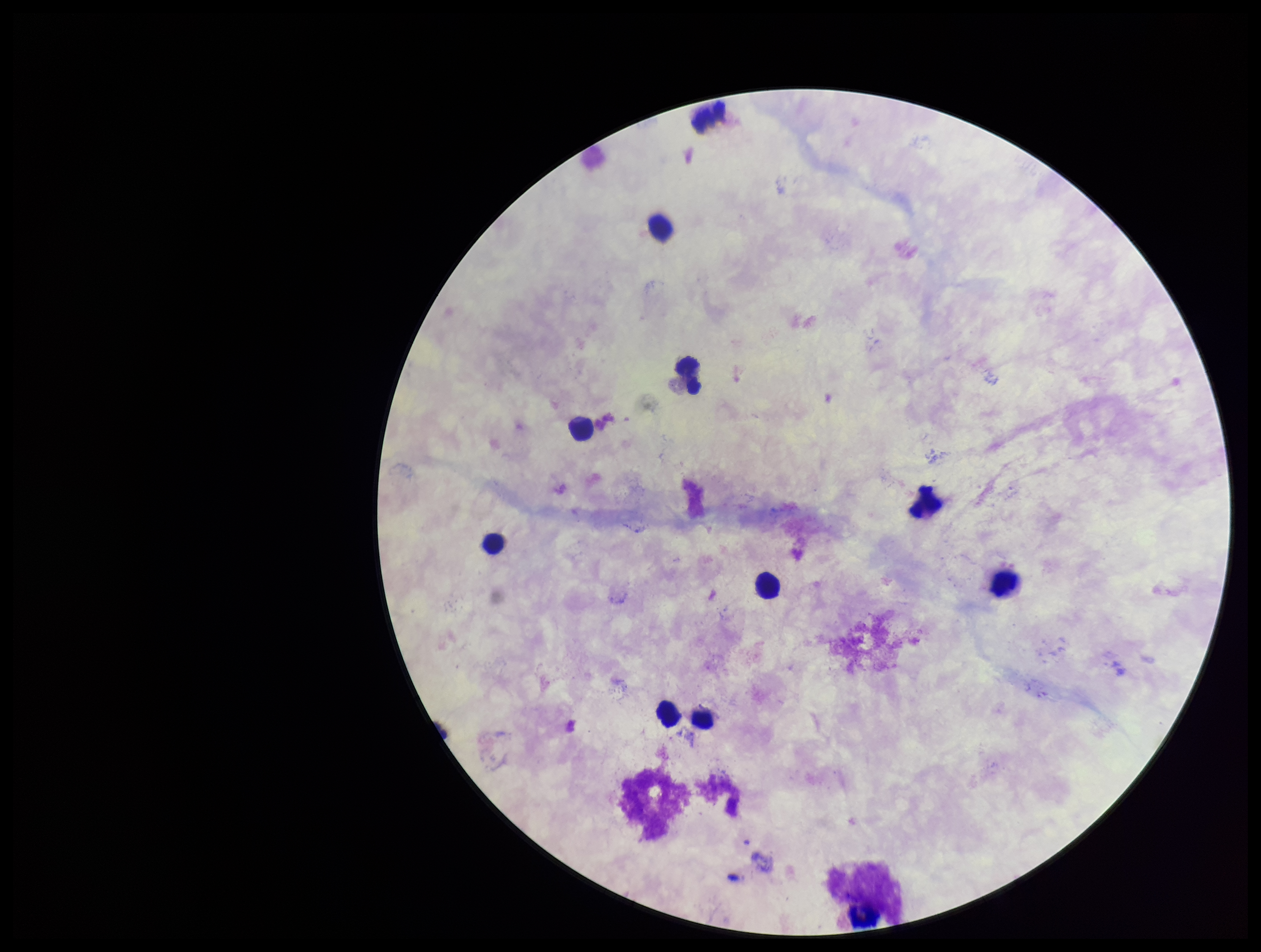
Preparation: thick blood smear. Patient malaria status: negative. Parasite count: 0. Photographed through the microscope eyepiece with a smartphone camera. Image is 1261×952 pixels. Stained with Giemsa. One field from this slide. Plasmodium parasites: none detected. Leukocyte count: 11.